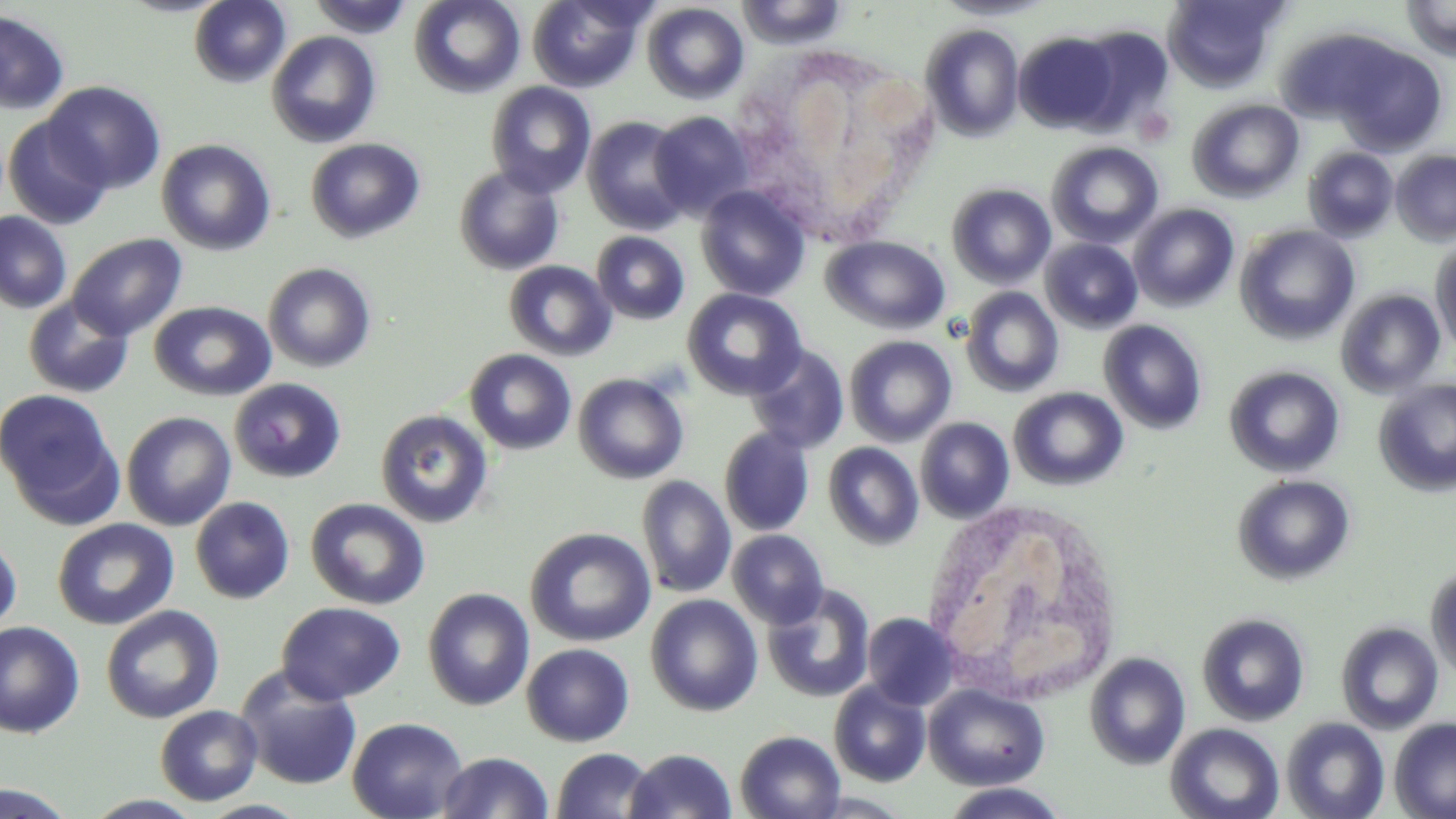
{
  "slide_level_diagnosis": "negative for blood parasites",
  "magnification": "1000x",
  "modality": "light microscopy",
  "uninfected_red_blood_cell_locations": "approximate bounding boxes as named x1/y1/x2/y2 corners in pixels: (x1=189, y1=0, x2=290, y2=87), (x1=308, y1=0, x2=414, y2=38), (x1=409, y1=0, x2=525, y2=97), (x1=527, y1=0, x2=646, y2=92), (x1=936, y1=0, x2=1054, y2=21), (x1=1162, y1=0, x2=1287, y2=92), (x1=1402, y1=0, x2=1456, y2=63), (x1=736, y1=1, x2=848, y2=49), (x1=642, y1=2, x2=749, y2=104), (x1=0, y1=9, x2=70, y2=114), (x1=920, y1=24, x2=1024, y2=141), (x1=1071, y1=24, x2=1175, y2=129), (x1=266, y1=30, x2=381, y2=148), (x1=1013, y1=31, x2=1120, y2=133), (x1=1335, y1=43, x2=1448, y2=155), (x1=43, y1=81, x2=166, y2=194), (x1=485, y1=82, x2=596, y2=198), (x1=1187, y1=99, x2=1304, y2=202), (x1=649, y1=111, x2=754, y2=220), (x1=3, y1=115, x2=112, y2=230), (x1=583, y1=116, x2=692, y2=235), (x1=305, y1=137, x2=425, y2=243), (x1=156, y1=138, x2=276, y2=255), (x1=1047, y1=142, x2=1163, y2=249), (x1=1303, y1=147, x2=1399, y2=242), (x1=1391, y1=150, x2=1456, y2=245), (x1=453, y1=165, x2=565, y2=276), (x1=947, y1=183, x2=1056, y2=289), (x1=696, y1=185, x2=810, y2=301), (x1=1128, y1=203, x2=1239, y2=311), (x1=0, y1=211, x2=72, y2=313), (x1=1235, y1=224, x2=1359, y2=344), (x1=592, y1=232, x2=689, y2=325), (x1=67, y1=233, x2=187, y2=340), (x1=821, y1=236, x2=951, y2=334), (x1=1430, y1=237, x2=1456, y2=356), (x1=1040, y1=238, x2=1143, y2=333), (x1=503, y1=260, x2=616, y2=361), (x1=262, y1=262, x2=377, y2=373), (x1=961, y1=287, x2=1064, y2=397), (x1=682, y1=288, x2=806, y2=400), (x1=1336, y1=289, x2=1445, y2=398), (x1=22, y1=295, x2=135, y2=399), (x1=148, y1=300, x2=276, y2=401), (x1=1099, y1=320, x2=1207, y2=434), (x1=844, y1=335, x2=957, y2=446), (x1=746, y1=345, x2=850, y2=454), (x1=465, y1=349, x2=576, y2=455), (x1=1225, y1=365, x2=1345, y2=478), (x1=573, y1=373, x2=689, y2=484), (x1=229, y1=378, x2=346, y2=483), (x1=1373, y1=379, x2=1456, y2=497), (x1=1009, y1=387, x2=1128, y2=491), (x1=1, y1=388, x2=123, y2=523), (x1=375, y1=409, x2=494, y2=528), (x1=121, y1=411, x2=237, y2=530), (x1=915, y1=417, x2=1014, y2=523), (x1=719, y1=427, x2=814, y2=537), (x1=823, y1=442, x2=924, y2=550), (x1=1232, y1=474, x2=1355, y2=585), (x1=636, y1=476, x2=736, y2=598), (x1=190, y1=496, x2=295, y2=604), (x1=306, y1=497, x2=430, y2=610), (x1=52, y1=518, x2=179, y2=630), (x1=525, y1=527, x2=655, y2=647), (x1=728, y1=529, x2=829, y2=629), (x1=0, y1=532, x2=21, y2=637), (x1=1426, y1=564, x2=1456, y2=684), (x1=762, y1=584, x2=876, y2=703), (x1=423, y1=588, x2=535, y2=710), (x1=646, y1=594, x2=763, y2=716), (x1=275, y1=601, x2=406, y2=705), (x1=101, y1=605, x2=224, y2=724), (x1=1197, y1=612, x2=1310, y2=726), (x1=862, y1=613, x2=960, y2=710), (x1=0, y1=621, x2=85, y2=738), (x1=1336, y1=622, x2=1444, y2=734), (x1=521, y1=643, x2=635, y2=747), (x1=1084, y1=652, x2=1191, y2=770), (x1=235, y1=668, x2=363, y2=790), (x1=829, y1=681, x2=931, y2=786), (x1=923, y1=683, x2=1050, y2=790), (x1=155, y1=705, x2=263, y2=806), (x1=347, y1=716, x2=468, y2=819), (x1=1281, y1=717, x2=1389, y2=819), (x1=1389, y1=717, x2=1456, y2=819), (x1=1165, y1=723, x2=1285, y2=819), (x1=735, y1=730, x2=846, y2=819), (x1=550, y1=748, x2=656, y2=819), (x1=624, y1=748, x2=737, y2=819), (x1=437, y1=751, x2=553, y2=818), (x1=0, y1=782, x2=81, y2=818), (x1=938, y1=783, x2=1072, y2=818), (x1=81, y1=793, x2=208, y2=818), (x1=196, y1=800, x2=313, y2=819)",
  "stain": "May-Grünwald-Giemsa",
  "image_size": "1456×819 pixels",
  "preparation": "thin blood film",
  "field_of_view": "one of a larger specimen",
  "white_blood_cell_locations": "approximate bounding boxes as named x1/y1/x2/y2 corners in pixels: (x1=719, y1=41, x2=945, y2=245), (x1=919, y1=497, x2=1128, y2=708)"
}